Outline each blood parasite and name the species.
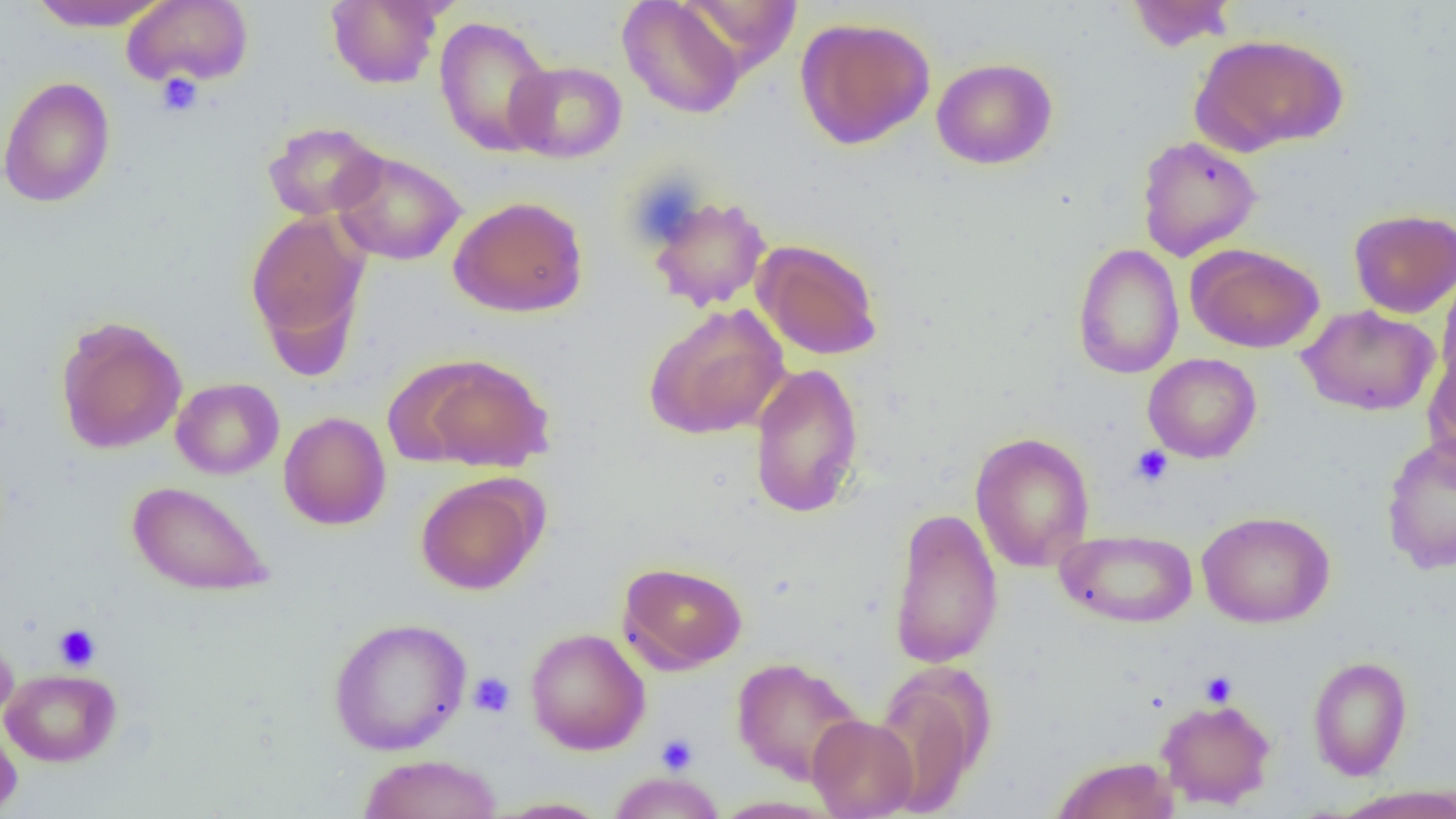

No blood parasites observed.

Approximate bounding boxes as (x1, y1, x2, y2) in pixels. Platelet locations: (156, 73, 204, 117), (1130, 445, 1174, 487), (54, 624, 100, 670), (1199, 671, 1237, 707), (468, 672, 515, 718), (656, 734, 699, 775). Uninfected red blood cell locations: (26, 0, 172, 31), (325, 0, 445, 89), (1125, 0, 1237, 52), (122, 1, 254, 87), (617, 1, 747, 119), (434, 15, 556, 157), (795, 16, 936, 150), (1192, 33, 1349, 154), (931, 57, 1058, 170), (505, 60, 627, 163), (0, 76, 116, 208), (262, 122, 385, 221), (1136, 135, 1262, 261), (330, 149, 467, 266), (647, 194, 773, 311), (449, 196, 588, 317), (1348, 208, 1456, 318), (246, 211, 370, 361), (752, 239, 884, 360), (1187, 243, 1324, 353), (1072, 244, 1184, 379), (1437, 267, 1456, 390), (643, 303, 789, 440), (1298, 305, 1439, 416), (55, 315, 188, 454), (1423, 347, 1456, 467), (1143, 353, 1261, 463), (407, 354, 555, 472), (749, 363, 865, 518), (171, 377, 284, 480), (278, 412, 391, 530), (969, 431, 1095, 572), (1380, 433, 1456, 576), (415, 473, 546, 595), (127, 481, 273, 597), (887, 506, 1003, 670), (1197, 510, 1335, 628), (1055, 528, 1198, 628), (618, 561, 748, 673), (328, 617, 471, 755), (524, 627, 651, 755), (0, 629, 19, 726), (1307, 655, 1413, 780), (731, 657, 865, 785), (871, 662, 994, 817), (0, 668, 122, 767), (1156, 696, 1276, 809), (807, 714, 919, 818), (0, 721, 22, 817), (359, 754, 504, 819), (1051, 755, 1180, 818), (608, 772, 725, 818), (1332, 787, 1456, 819), (490, 797, 613, 818). Slide-level diagnosis: no evidence of blood parasites. Thin blood smear. Light microscopy. Single field of view. Captured at 1000x magnification. Image is 1456×819 pixels.